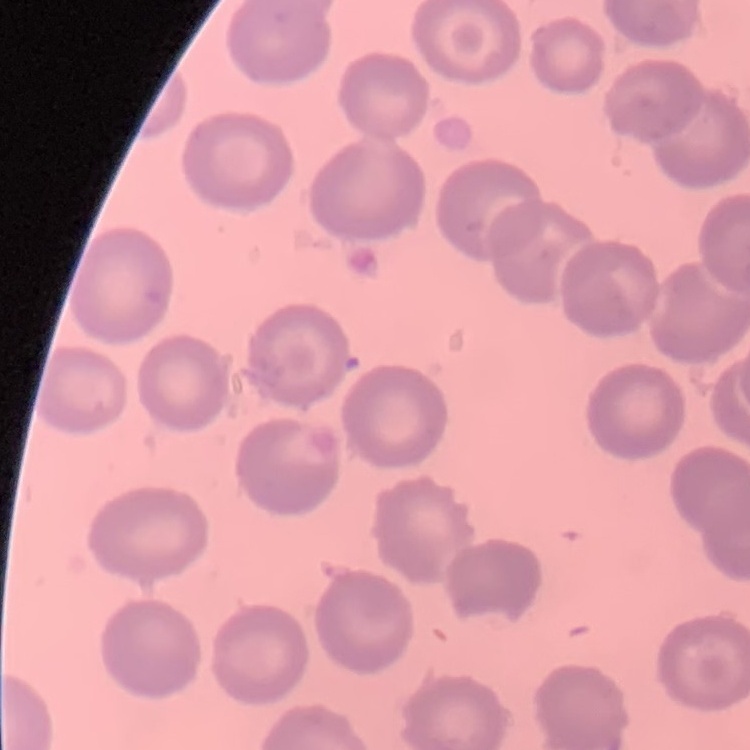
{
  "red_blood_cell_morphology": "no rouleaux formation",
  "stain": "Field's or Giemsa",
  "image_type": "one tile cut from a larger photomicrograph",
  "preparation": "thin blood film"
}